Describe the morphology of the erythrocytes.
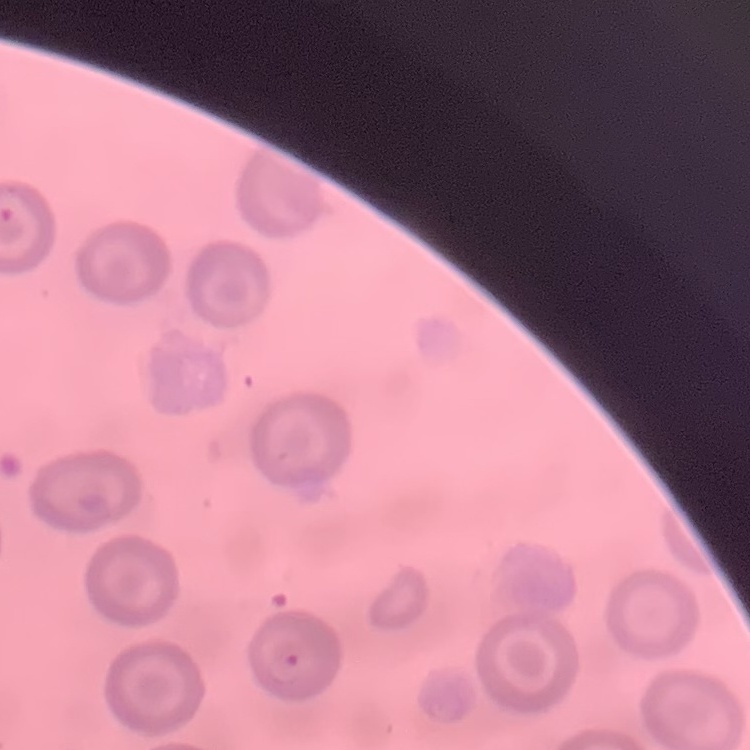
They show no rouleaux formation.

{
  "stain": "Field's or Giemsa",
  "image_type": "square crop of a larger photomicrograph",
  "preparation": "thin blood smear"
}